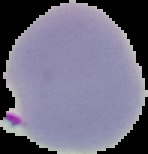 From a thin blood smear. Result: Plasmodium parasites detected. Image is 148×154 pixels. Cell region segmented out of the field of view; the surrounding area is masked to black.